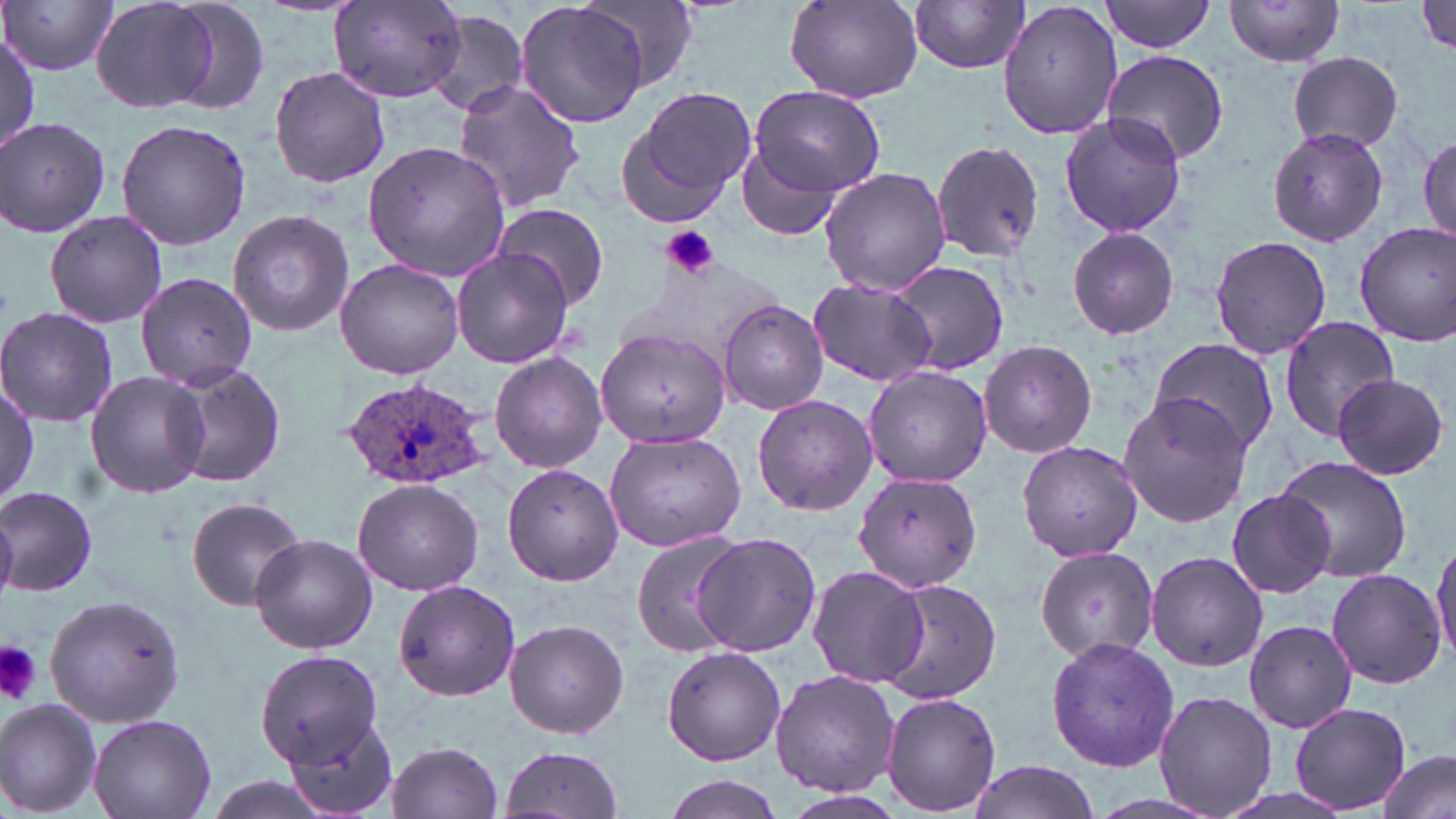
Summary:
  - Coordinate format: approximate bounding boxes as (x1, y1, x2, y2) in pixels
  - Uninfected red blood cell locations: (4, 0, 118, 75), (90, 0, 223, 115), (160, 0, 274, 113), (1100, 0, 1218, 54), (1222, 0, 1348, 67), (1411, 0, 1456, 61), (327, 1, 467, 103), (516, 1, 656, 128), (579, 1, 700, 91), (909, 1, 1030, 75), (785, 2, 922, 102), (998, 2, 1125, 141), (425, 9, 530, 117), (1, 29, 41, 153), (1100, 49, 1229, 165), (1286, 51, 1405, 155), (268, 66, 392, 188), (452, 80, 586, 212), (627, 85, 756, 214), (749, 86, 884, 199), (1058, 111, 1185, 238), (1, 117, 112, 239), (116, 120, 252, 251), (1267, 125, 1389, 247), (1418, 131, 1453, 244), (931, 138, 1045, 261), (363, 141, 513, 281), (735, 145, 844, 241), (819, 167, 952, 296), (493, 202, 608, 311), (227, 209, 354, 337), (44, 212, 168, 326), (1355, 221, 1456, 347), (1068, 227, 1180, 339), (1209, 235, 1331, 359), (451, 247, 574, 368), (335, 258, 464, 380), (889, 259, 1010, 376), (135, 270, 264, 398), (807, 277, 938, 387), (717, 300, 828, 416), (0, 306, 118, 427), (1277, 316, 1401, 439), (597, 324, 732, 450), (1148, 338, 1281, 463), (979, 339, 1098, 458), (492, 353, 609, 473), (164, 361, 288, 488), (865, 364, 991, 487), (84, 370, 211, 500), (1331, 374, 1448, 480), (1, 376, 36, 507), (1118, 390, 1252, 527), (751, 393, 878, 516), (603, 429, 746, 552), (1016, 438, 1142, 561), (1274, 455, 1413, 581), (503, 464, 623, 586), (855, 471, 982, 592), (353, 479, 482, 596), (0, 485, 98, 598), (1227, 490, 1336, 600), (0, 497, 17, 604), (185, 497, 305, 611), (631, 531, 744, 656), (691, 532, 822, 656), (249, 533, 377, 653), (1432, 535, 1456, 666), (1036, 546, 1160, 663), (1145, 551, 1269, 673), (806, 565, 925, 687), (1327, 568, 1448, 689), (873, 576, 1002, 703), (394, 578, 521, 702), (44, 594, 185, 725), (505, 618, 628, 739), (1241, 620, 1356, 733), (1203, 633, 1324, 772), (1045, 636, 1179, 772), (661, 644, 787, 766), (254, 648, 382, 766), (770, 670, 898, 797), (1153, 690, 1278, 818), (880, 691, 1001, 815), (0, 699, 103, 817), (1291, 703, 1408, 814), (88, 713, 217, 819), (283, 715, 399, 819), (385, 740, 503, 819), (499, 745, 626, 818), (1375, 750, 1453, 819), (964, 760, 1100, 819), (661, 776, 782, 818), (784, 789, 909, 819)
  - Plasmodium ovale-infected red blood cell locations: (340, 375, 490, 490)
  - Platelet locations: (662, 226, 721, 279), (0, 643, 44, 706)
  - Slide-level diagnosis: Plasmodium ovale
  - Field of view: single
  - Image size: 1456×819 pixels
  - Stain: May-Grünwald-Giemsa
  - Modality: optical microscopy
  - Preparation: thin blood smear
  - Magnification: 1000x